Classify this cell by malaria status.
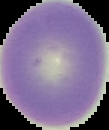
Uninfected.

Summary:
  - Image type: segmented cell region with the area outside set to black
  - Image size: 109×130 pixels
  - Preparation: thin blood smear